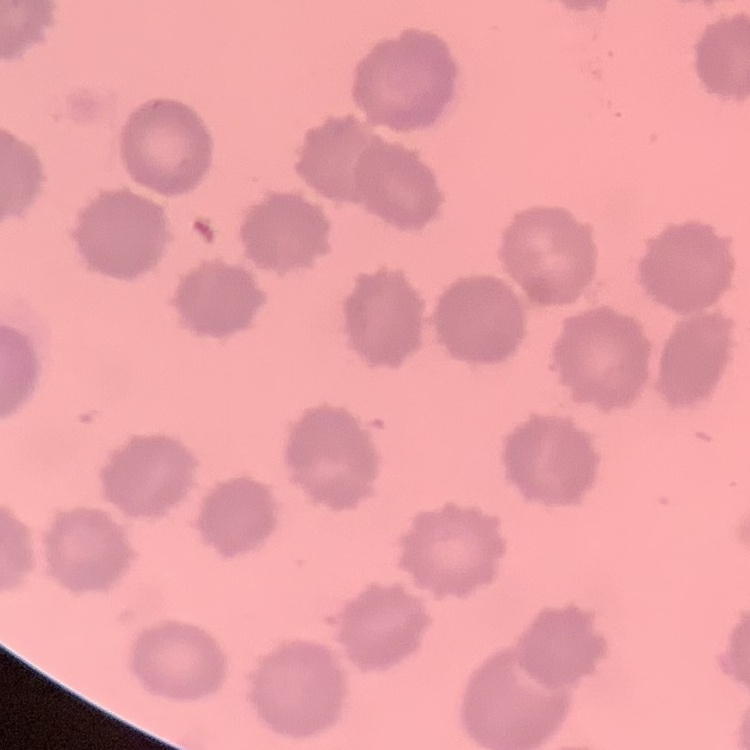

Summary:
  - Red blood cell morphology: no rouleaux formation
  - Preparation: thin blood film
  - Stain: Field's or Giemsa
  - Image type: square crop of a larger photomicrograph